Assess this cell for malaria.
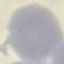

It is uninfected.

image_type: automatically extracted cell patch, resized to 64 × 64 pixels
capture: smartphone through the microscope eyepiece
stain: Giemsa
preparation: thin blood smear